Describe the morphology of the red blood cells.
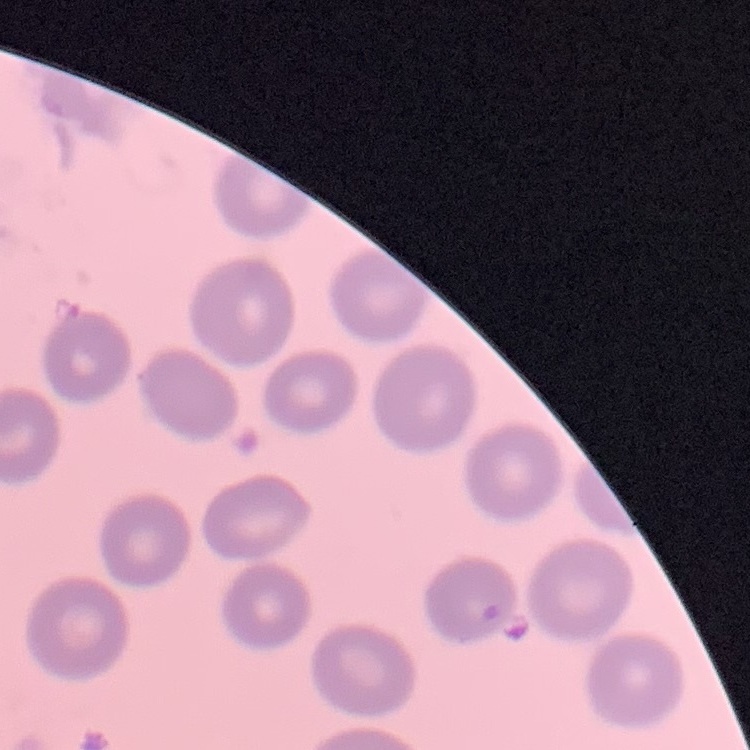
They show no rouleaux formation.

Summary:
  - Image type: square crop of a larger photomicrograph
  - Stain: Field's or Giemsa
  - Preparation: thin peripheral smear